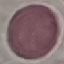
malaria status = uninfected
stain = Giemsa
preparation = thin blood smear
image type = cell patch, automatically extracted from a larger field of view and resized to 64 × 64 pixels
capture = smartphone through the microscope eyepiece